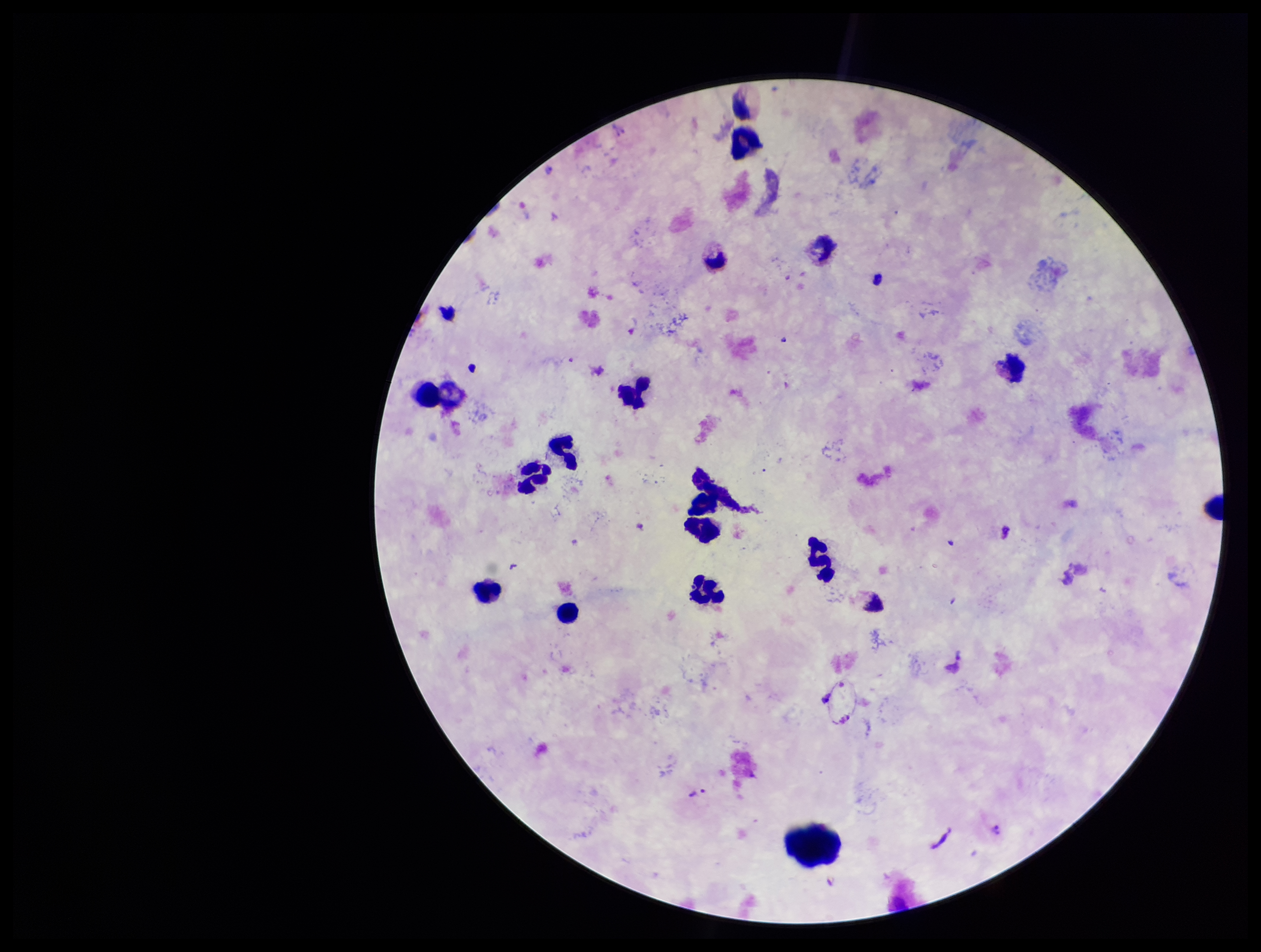
Summary:
  - Leukocyte count: 13
  - Species reported for this patient: Plasmodium vivax
  - Capture: smartphone photograph through the microscope eyepiece
  - Parasite count: 1
  - Preparation: thick blood smear
  - Field of view: one from this slide
  - Stain: Giemsa
  - Plasmodium parasites: detected
  - Patient malaria status: positive
  - Image size: 1261×952 pixels